Assess the morphology of the erythrocytes.
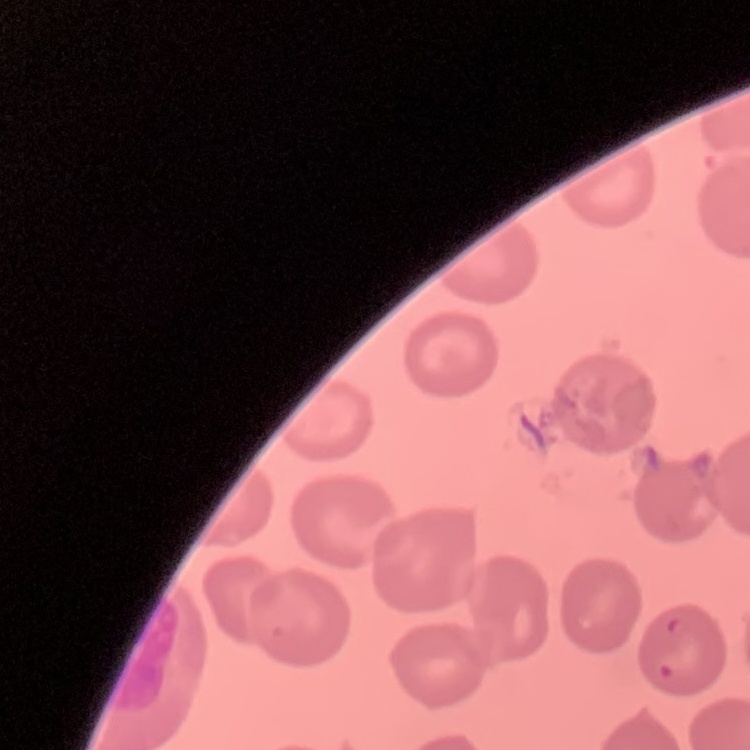

No rouleaux formation.

Summary:
  - Image type: one tile cut from a larger photomicrograph
  - Stain: Field's or Giemsa
  - Preparation: thin blood film